Classify this cell by malaria status.
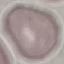

It is uninfected.

Cell patch, automatically extracted from a larger field of view and resized to 64 × 64 pixels. Acquired by smartphone through the microscope eyepiece. Giemsa-stained preparation. Thin blood smear.